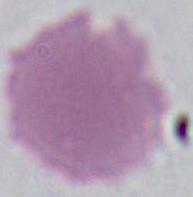

{
  "magnification": "1000x",
  "identification": "erythrocyte",
  "modality": "micrograph"
}